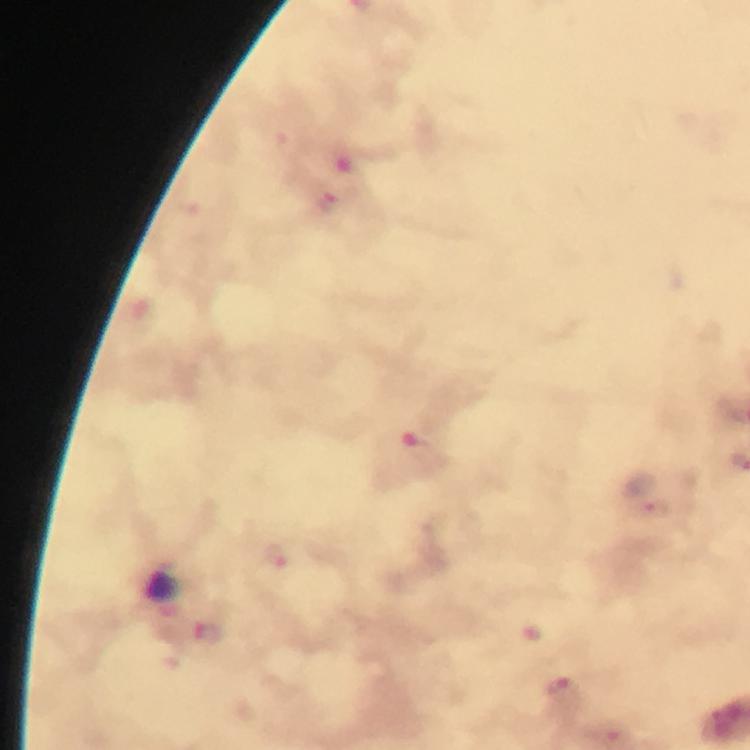

Approximate centers as [x, y] in pixels. Plasmodium parasite locations: [329, 203], [418, 445], [657, 508], [276, 554], [208, 633], [562, 690]. Image is 750×750 pixels. Photographed with a smartphone mounted on the microscope. Thick blood film. Giemsa-stained preparation. At 100x magnification. From a diagnostic examination for malaria. Immersion oil applied. Cropped region of a single field of view.